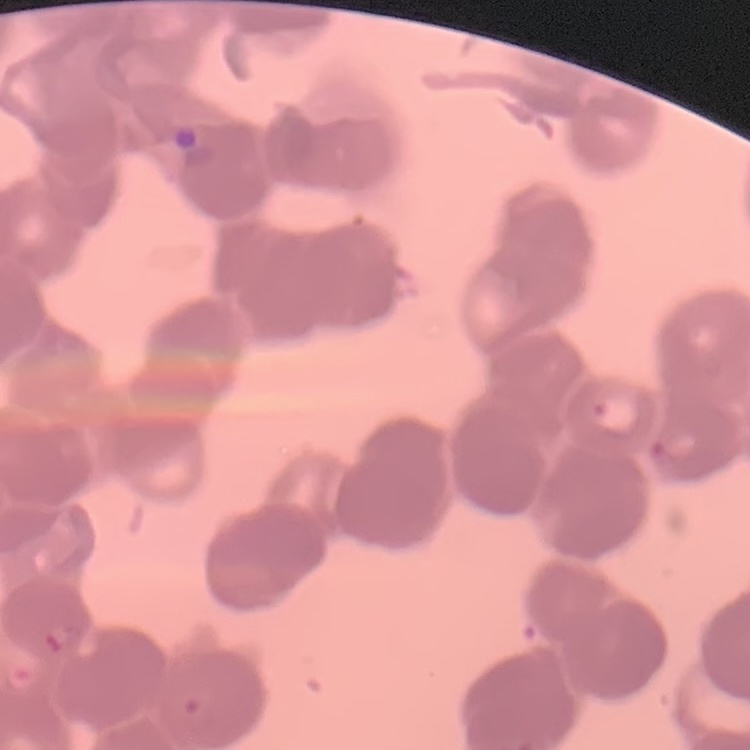

red blood cell morphology = rouleaux formation
preparation = thin blood smear
stain = Field's or Giemsa
image type = one tile cut from a larger photomicrograph